Name the parasite shown.
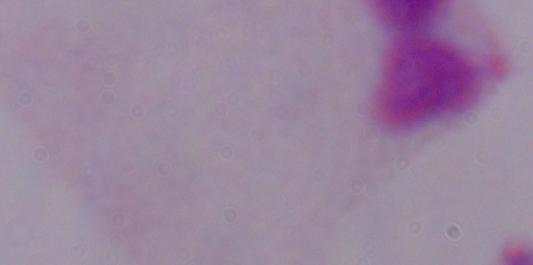

This is a trichomonad.

Micrograph. 1000x magnification.